Identify the parasite.
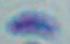

Toxoplasma gondii.

Micrograph. Captured at 1000x magnification.